Report the malaria status of this cell.
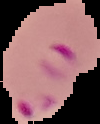

It is parasitized.

{
  "preparation": "thin blood smear",
  "image_size": "100×124 pixels",
  "image_type": "segmented cell region with the area outside set to black"
}